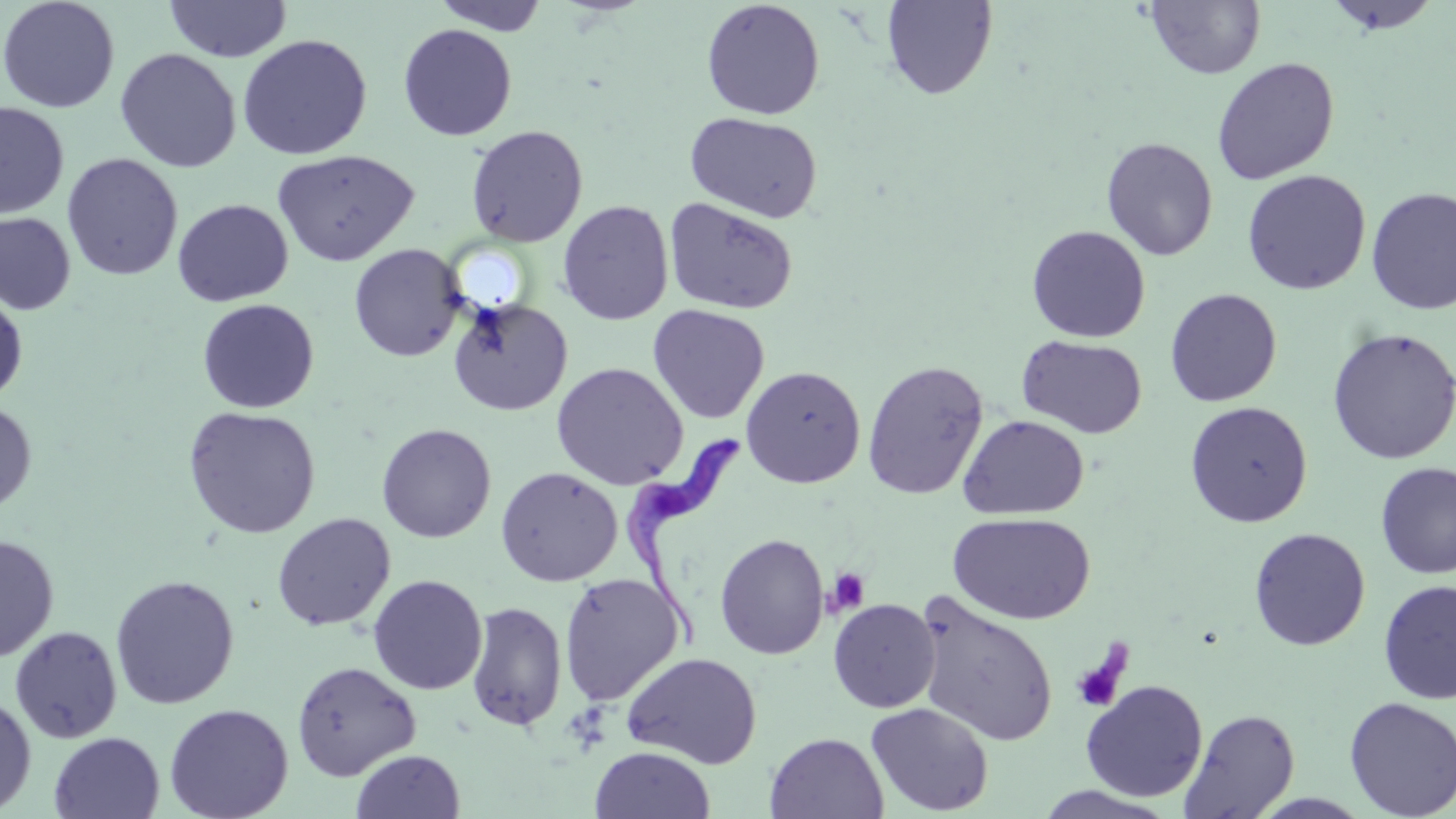
slide-level diagnosis = Trypanosoma brucei
platelet locations = approximate bounding boxes as named x1/y1/x2/y2 corners in pixels: (x1=826, y1=567, x2=870, y2=617), (x1=1071, y1=650, x2=1128, y2=714)
field of view = one of a larger specimen
uninfected red blood cell locations = approximate bounding boxes as named x1/y1/x2/y2 corners in pixels: (x1=0, y1=0, x2=120, y2=113), (x1=164, y1=0, x2=293, y2=62), (x1=430, y1=0, x2=551, y2=36), (x1=881, y1=0, x2=998, y2=100), (x1=1322, y1=0, x2=1443, y2=35), (x1=701, y1=1, x2=825, y2=120), (x1=1145, y1=1, x2=1266, y2=79), (x1=398, y1=23, x2=517, y2=141), (x1=236, y1=34, x2=373, y2=160), (x1=115, y1=48, x2=241, y2=172), (x1=1212, y1=57, x2=1339, y2=185), (x1=0, y1=102, x2=69, y2=220), (x1=686, y1=112, x2=823, y2=223), (x1=465, y1=124, x2=588, y2=247), (x1=1100, y1=137, x2=1218, y2=261), (x1=272, y1=149, x2=419, y2=266), (x1=61, y1=153, x2=183, y2=281), (x1=1241, y1=169, x2=1371, y2=295), (x1=1365, y1=186, x2=1456, y2=315), (x1=663, y1=197, x2=799, y2=315), (x1=173, y1=199, x2=293, y2=306), (x1=183, y1=200, x2=308, y2=412), (x1=557, y1=200, x2=674, y2=325), (x1=0, y1=211, x2=77, y2=316), (x1=1026, y1=225, x2=1150, y2=342), (x1=348, y1=244, x2=467, y2=362), (x1=0, y1=287, x2=28, y2=406), (x1=1165, y1=288, x2=1283, y2=407), (x1=448, y1=298, x2=573, y2=416), (x1=197, y1=299, x2=319, y2=413), (x1=647, y1=305, x2=769, y2=424), (x1=1326, y1=327, x2=1456, y2=465), (x1=1017, y1=335, x2=1147, y2=439), (x1=862, y1=360, x2=988, y2=500), (x1=551, y1=362, x2=688, y2=490), (x1=741, y1=366, x2=865, y2=488), (x1=0, y1=399, x2=37, y2=515), (x1=1185, y1=401, x2=1313, y2=528), (x1=183, y1=405, x2=321, y2=539), (x1=959, y1=415, x2=1090, y2=520), (x1=376, y1=424, x2=497, y2=542), (x1=1375, y1=462, x2=1456, y2=579), (x1=496, y1=467, x2=622, y2=586), (x1=948, y1=512, x2=1095, y2=625), (x1=272, y1=513, x2=396, y2=631), (x1=1248, y1=527, x2=1370, y2=651), (x1=0, y1=533, x2=59, y2=663), (x1=714, y1=533, x2=829, y2=659), (x1=559, y1=572, x2=684, y2=706), (x1=110, y1=574, x2=240, y2=709), (x1=368, y1=574, x2=488, y2=695), (x1=1378, y1=580, x2=1456, y2=704), (x1=914, y1=594, x2=1059, y2=747), (x1=828, y1=599, x2=941, y2=713), (x1=465, y1=601, x2=567, y2=732), (x1=9, y1=625, x2=123, y2=743), (x1=621, y1=651, x2=762, y2=768), (x1=291, y1=661, x2=421, y2=780), (x1=1080, y1=680, x2=1208, y2=802), (x1=0, y1=694, x2=36, y2=814), (x1=1344, y1=696, x2=1456, y2=818), (x1=865, y1=702, x2=994, y2=816), (x1=164, y1=703, x2=294, y2=819), (x1=1179, y1=708, x2=1300, y2=818), (x1=49, y1=731, x2=164, y2=819), (x1=764, y1=732, x2=888, y2=818), (x1=590, y1=745, x2=716, y2=819), (x1=350, y1=749, x2=466, y2=818), (x1=1033, y1=786, x2=1178, y2=818)
stain = May-Grünwald-Giemsa
preparation = thin blood film
image size = 1456×819 pixels
magnification = 1000x
Trypanosoma brucei locations = approximate bounding boxes as named x1/y1/x2/y2 corners in pixels: (x1=620, y1=428, x2=742, y2=654)
modality = light microscopy